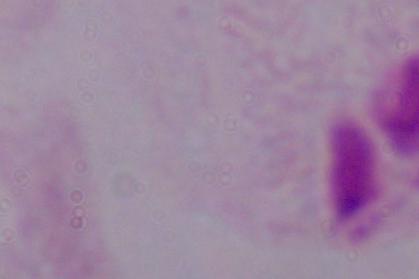
magnification = 1000x
identification = trichomonad
modality = photomicrograph